Classify the preparation.
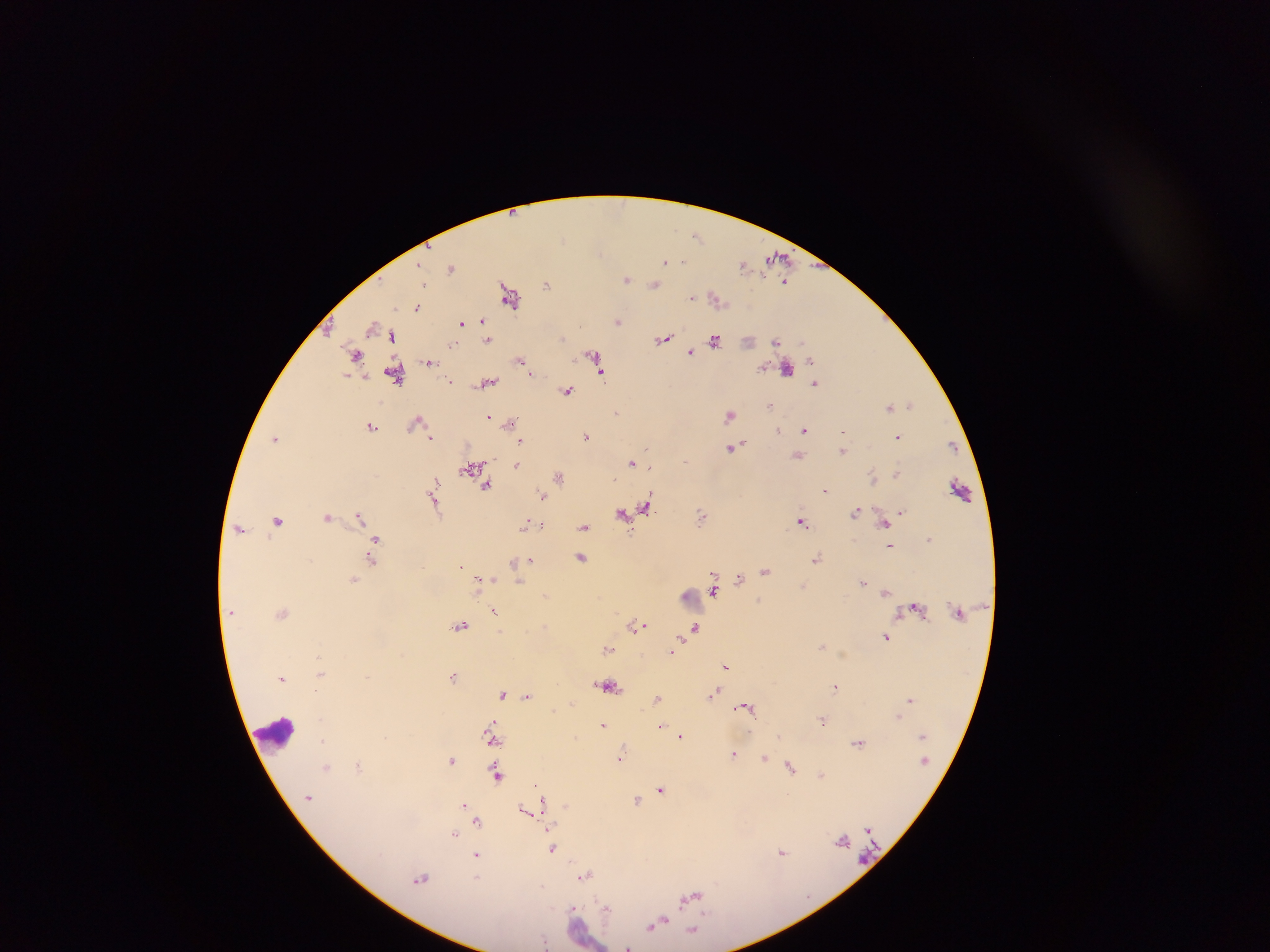

Thick blood smear.

image size = 1270×952 pixels
capture = mobile-phone photograph through a microscope
country = Ghana
leukocyte locations = approximate centers as {x, y} in pixels: {275, 733}
field of view = single
Plasmodium parasite locations = approximate centers as {x, y} in pixels: {697, 235}, {777, 258}, {665, 262}, {743, 265}, {420, 266}, {452, 268}, {628, 279}, {784, 282}, {547, 284}, {655, 284}, {512, 295}, {693, 297}, {717, 298}, {418, 306}, {463, 321}, {482, 321}, {618, 321}, {469, 323}, {327, 324}, {373, 327}, {485, 332}, {392, 336}, {487, 338}, {663, 338}, {715, 340}, {749, 340}, {777, 340}, {453, 344}, {691, 351}, {357, 355}, {596, 359}, {521, 360}, {430, 361}, {787, 367}, {396, 372}, {346, 375}, {451, 380}, {488, 382}, {816, 383}, {567, 390}, {891, 405}, {900, 405}, {911, 405}, {770, 406}, {615, 411}, {730, 415}, {489, 417}, {416, 421}, {510, 423}, {372, 425}, {779, 430}, {804, 431}, {587, 435}, {898, 436}, {431, 437}, {275, 438}, {521, 441}, {952, 444}, {733, 446}, {647, 448}, {843, 449}, {798, 454}, {631, 462}, {517, 464}, {473, 467}, {897, 473}, {559, 475}, {874, 476}, {436, 481}, {487, 484}, {825, 488}, {960, 490}, {543, 494}, {434, 499}, {647, 505}, {902, 511}, {857, 512}, {623, 514}, {702, 515}, {328, 517}, {359, 517}, {277, 520}, {801, 520}, {886, 521}, {527, 523}, {585, 526}, {240, 527}, {377, 538}, {929, 538}, {374, 545}, {890, 546}, {582, 557}, {372, 559}, {817, 559}, {530, 560}, {515, 561}, {521, 564}, {461, 567}, {766, 571}, {739, 577}, {354, 579}, {492, 579}, {520, 582}, {863, 582}, {480, 583}, {804, 586}, {714, 589}, {885, 592}, {545, 596}, {759, 598}, {916, 608}, {495, 611}, {460, 625}, {638, 625}, {697, 627}, {886, 636}, {822, 646}, {607, 648}, {672, 652}, {726, 666}, {321, 672}, {369, 676}, {454, 676}, {283, 678}, {608, 686}, {836, 686}, {716, 691}, {504, 693}, {527, 694}, {657, 698}, {910, 699}, {745, 706}, {898, 717}, {823, 719}, {495, 721}, {604, 723}, {661, 725}, {781, 734}, {681, 736}, {493, 740}, {322, 741}, {858, 741}, {734, 752}, {620, 757}, {766, 757}, {452, 760}, {327, 766}, {360, 766}, {791, 767}, {497, 773}, {822, 774}, {662, 788}, {544, 799}, {637, 799}, {465, 803}, {567, 804}, {531, 808}, {526, 811}, {478, 821}, {869, 827}, {455, 835}, {844, 841}, {553, 847}, {783, 851}, {477, 853}, {585, 875}, {421, 878}, {479, 878}, {691, 897}, {609, 907}, {574, 909}, {657, 923}, {693, 930}, {546, 941}, {629, 945}